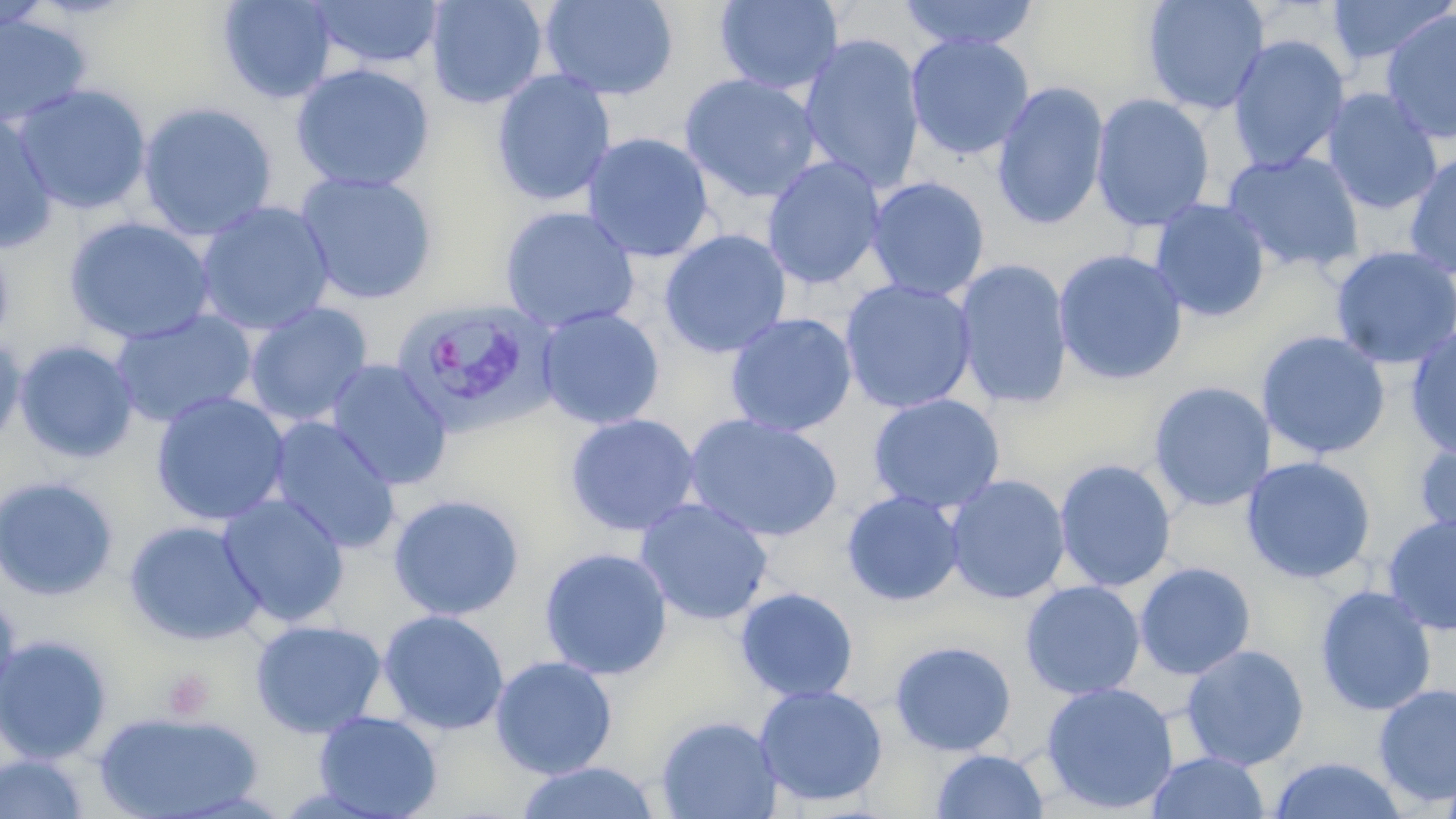
Approximate bounding boxes as named x1/y1/x2/y2 corners in pixels. Platelet locations: (x1=162, y1=669, x2=215, y2=720). Plasmodium vivax-infected red blood cell locations: (x1=393, y1=297, x2=556, y2=436). Uninfected red blood cell locations: (x1=425, y1=0, x2=548, y2=109), (x1=538, y1=0, x2=679, y2=101), (x1=898, y1=0, x2=1041, y2=52), (x1=1141, y1=0, x2=1271, y2=116), (x1=1326, y1=0, x2=1453, y2=65), (x1=217, y1=1, x2=338, y2=104), (x1=309, y1=1, x2=445, y2=71), (x1=714, y1=1, x2=843, y2=95), (x1=0, y1=3, x2=53, y2=38), (x1=1380, y1=9, x2=1456, y2=144), (x1=0, y1=12, x2=93, y2=130), (x1=799, y1=33, x2=925, y2=193), (x1=905, y1=33, x2=1034, y2=160), (x1=1227, y1=34, x2=1350, y2=174), (x1=290, y1=63, x2=436, y2=194), (x1=491, y1=69, x2=617, y2=207), (x1=680, y1=73, x2=822, y2=204), (x1=991, y1=81, x2=1109, y2=231), (x1=12, y1=83, x2=152, y2=215), (x1=1321, y1=87, x2=1443, y2=216), (x1=1090, y1=93, x2=1215, y2=232), (x1=137, y1=101, x2=279, y2=240), (x1=0, y1=113, x2=59, y2=253), (x1=582, y1=132, x2=716, y2=263), (x1=1221, y1=150, x2=1365, y2=274), (x1=1403, y1=150, x2=1456, y2=279), (x1=762, y1=156, x2=886, y2=289), (x1=293, y1=171, x2=439, y2=305), (x1=865, y1=176, x2=990, y2=302), (x1=1149, y1=199, x2=1271, y2=322), (x1=195, y1=200, x2=335, y2=335), (x1=499, y1=205, x2=640, y2=332), (x1=63, y1=216, x2=216, y2=346), (x1=659, y1=228, x2=792, y2=359), (x1=0, y1=237, x2=14, y2=351), (x1=1330, y1=245, x2=1456, y2=370), (x1=1053, y1=248, x2=1188, y2=385), (x1=953, y1=258, x2=1073, y2=409), (x1=839, y1=278, x2=977, y2=414), (x1=244, y1=302, x2=373, y2=427), (x1=536, y1=306, x2=665, y2=430), (x1=110, y1=309, x2=258, y2=428), (x1=724, y1=312, x2=858, y2=437), (x1=1405, y1=323, x2=1456, y2=459), (x1=1257, y1=330, x2=1391, y2=460), (x1=0, y1=334, x2=27, y2=454), (x1=14, y1=340, x2=139, y2=463), (x1=325, y1=359, x2=453, y2=491), (x1=1148, y1=381, x2=1272, y2=512), (x1=150, y1=391, x2=291, y2=527), (x1=867, y1=393, x2=1005, y2=514), (x1=683, y1=412, x2=844, y2=543), (x1=564, y1=413, x2=701, y2=537), (x1=267, y1=416, x2=402, y2=554), (x1=1412, y1=436, x2=1456, y2=549), (x1=1240, y1=455, x2=1377, y2=585), (x1=1054, y1=459, x2=1177, y2=592), (x1=944, y1=474, x2=1071, y2=605), (x1=0, y1=476, x2=119, y2=601), (x1=841, y1=490, x2=964, y2=607), (x1=217, y1=493, x2=351, y2=628), (x1=387, y1=493, x2=525, y2=621), (x1=635, y1=498, x2=774, y2=626), (x1=1381, y1=514, x2=1456, y2=636), (x1=124, y1=519, x2=265, y2=646), (x1=538, y1=547, x2=673, y2=680), (x1=1134, y1=562, x2=1256, y2=680), (x1=1020, y1=580, x2=1146, y2=699), (x1=1315, y1=585, x2=1437, y2=716), (x1=734, y1=587, x2=859, y2=703), (x1=0, y1=594, x2=22, y2=713), (x1=377, y1=609, x2=510, y2=736), (x1=250, y1=619, x2=387, y2=738), (x1=0, y1=634, x2=113, y2=764), (x1=889, y1=640, x2=1016, y2=756), (x1=1180, y1=644, x2=1309, y2=771), (x1=490, y1=656, x2=618, y2=779), (x1=1040, y1=680, x2=1179, y2=815), (x1=754, y1=683, x2=889, y2=808), (x1=1373, y1=683, x2=1456, y2=807), (x1=313, y1=710, x2=443, y2=819), (x1=92, y1=712, x2=265, y2=819), (x1=655, y1=714, x2=781, y2=819), (x1=930, y1=749, x2=1050, y2=819), (x1=1146, y1=751, x2=1270, y2=819), (x1=0, y1=753, x2=93, y2=819), (x1=1266, y1=756, x2=1409, y2=818), (x1=513, y1=761, x2=661, y2=818). Slide-level diagnosis: Plasmodium vivax. Single field of view. May-Grünwald-Giemsa stain. Image is 1456×819 pixels. Thin blood smear. Optical microscopy. 1000x magnification.